Name the blood parasite species.
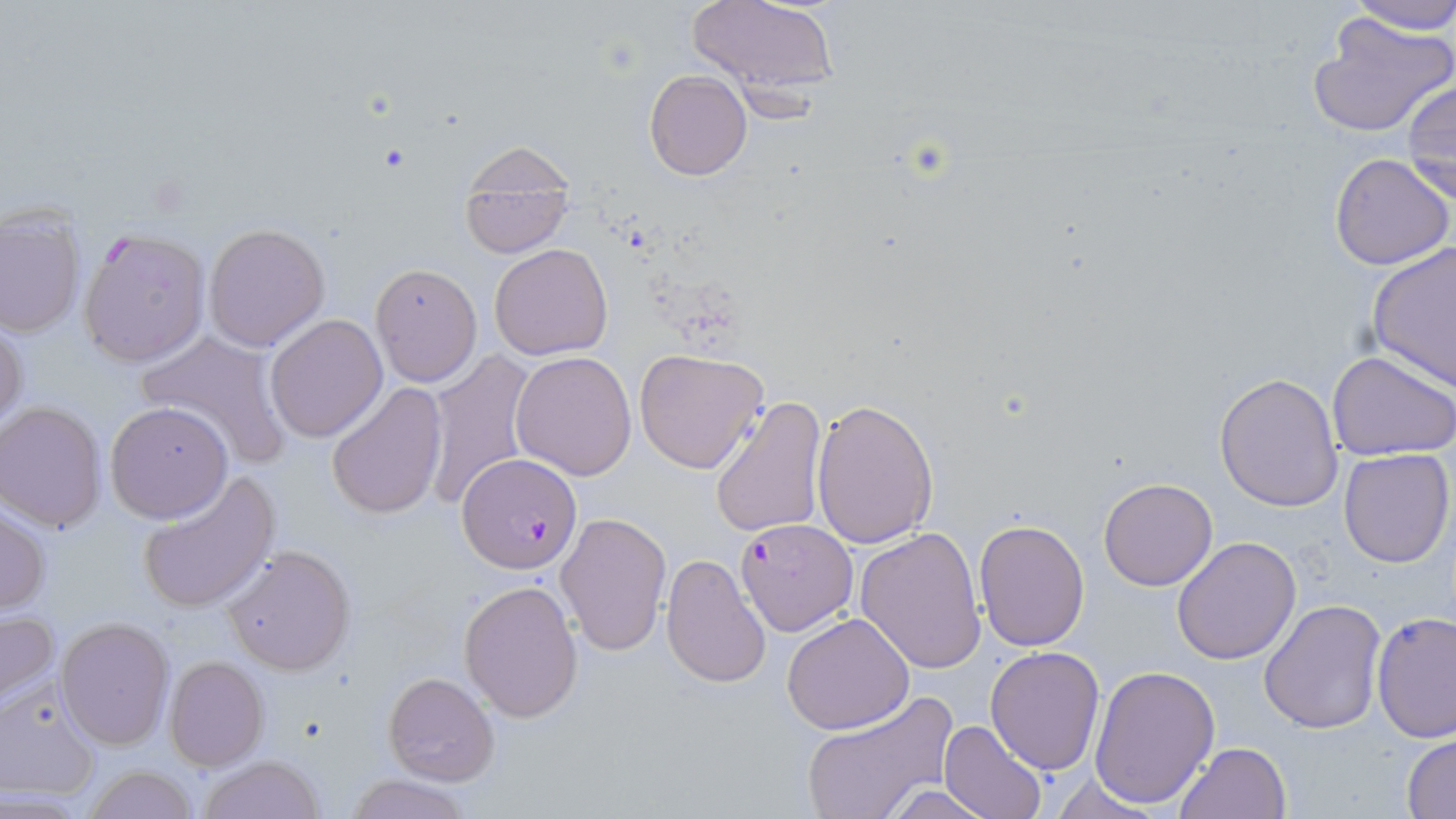
Plasmodium falciparum.

Approximate bounding boxes as (x1,y1)-(x2,y2) corner pairs in pixels. Uninfected red blood cell locations: (685,0)-(841,102), (1345,0)-(1456,36), (1306,11)-(1456,140), (644,69)-(752,180), (1403,81)-(1455,203), (456,153)-(579,261), (1330,153)-(1454,271), (0,206)-(85,339), (203,223)-(331,351), (1367,242)-(1455,389), (490,243)-(613,360), (370,263)-(481,387), (263,313)-(388,442), (0,314)-(27,435), (134,330)-(292,469), (633,347)-(770,474), (422,350)-(538,512), (1328,350)-(1456,460), (511,351)-(639,480), (1214,371)-(1343,512), (326,383)-(448,521), (710,394)-(828,539), (811,398)-(939,549), (105,401)-(233,523), (0,402)-(108,532), (1338,447)-(1454,568), (134,471)-(281,614), (1099,476)-(1218,591), (0,503)-(51,616), (555,511)-(670,657), (974,519)-(1090,652), (854,528)-(987,674), (1171,536)-(1301,664), (222,545)-(356,676), (661,552)-(771,687), (458,579)-(583,723), (1258,600)-(1386,735), (0,606)-(61,713), (1371,610)-(1455,741), (782,613)-(914,734), (56,617)-(174,751), (985,646)-(1104,775), (163,656)-(270,771), (1088,664)-(1220,808), (383,672)-(500,786), (0,679)-(103,801), (798,690)-(957,819), (940,721)-(1047,819), (1403,735)-(1456,816), (1175,741)-(1292,819), (197,755)-(329,818), (82,764)-(200,819), (344,773)-(476,819), (1049,774)-(1169,818), (878,782)-(991,819). Plasmodium falciparum-infected red blood cell locations: (78,228)-(211,369), (458,452)-(582,572), (733,517)-(858,636). Light microscopy. May-Grünwald-Giemsa stain. Thin blood film. Image is 1456×819 pixels. One field of a larger specimen. 1000x magnification.